Assess this cell for malaria.
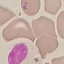
It is uninfected.

Giemsa-stained preparation. Cell patch, automatically extracted from a larger field of view and resized to 64 × 64 pixels. Photographed with a smartphone camera at the microscope eyepiece. Thin blood film.